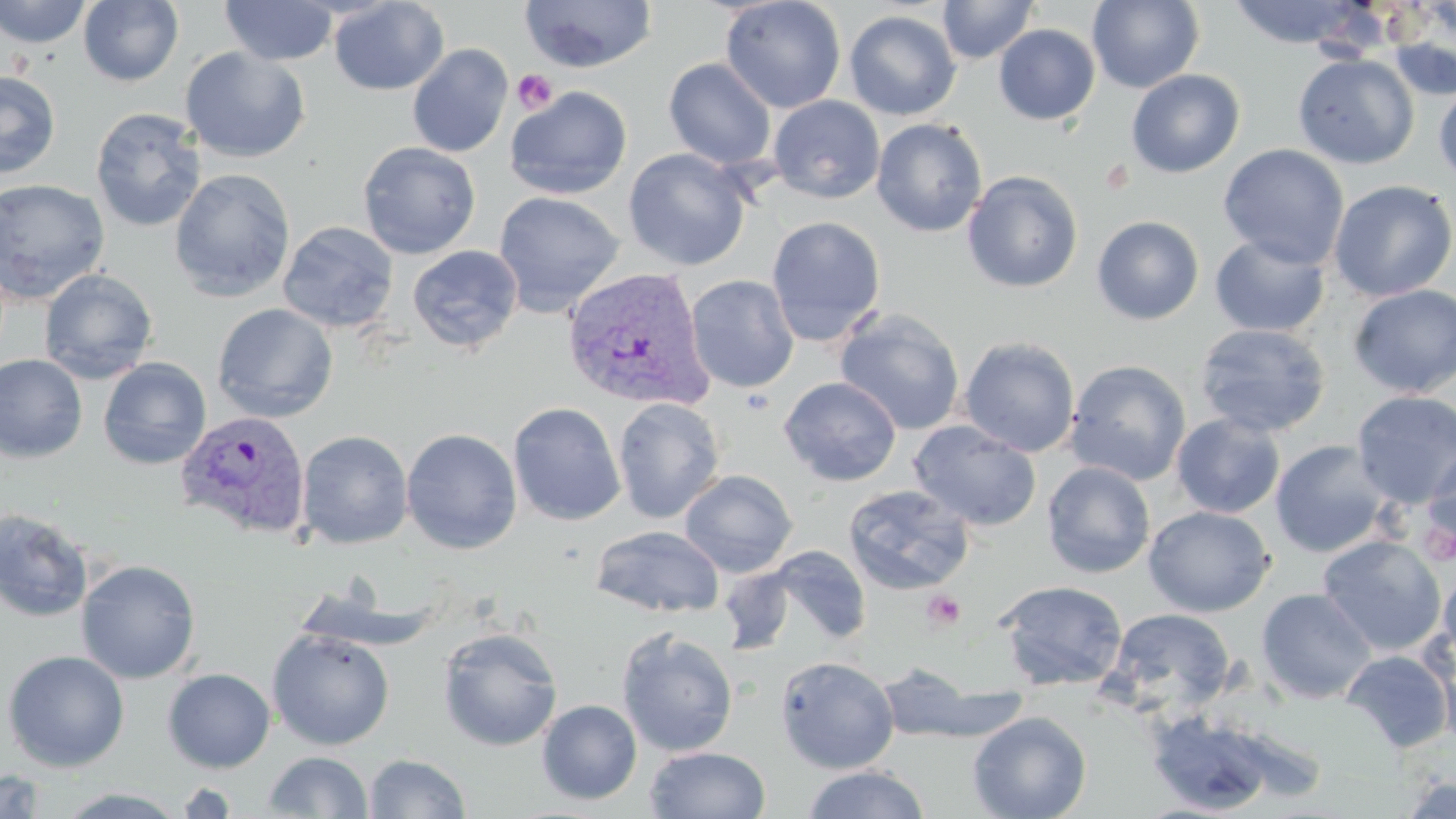
Approximate bounding boxes as (x1, y1, x2, y2) in pixels. Uninfected red blood cell locations: (0, 0, 93, 49), (77, 0, 183, 87), (328, 0, 449, 96), (519, 0, 657, 74), (720, 0, 846, 114), (937, 0, 1039, 65), (1087, 0, 1205, 94), (219, 1, 339, 66), (1228, 1, 1365, 48), (1385, 1, 1456, 100), (844, 9, 961, 120), (994, 24, 1100, 125), (407, 44, 513, 158), (180, 46, 311, 164), (1293, 53, 1419, 169), (663, 57, 777, 171), (1126, 69, 1245, 178), (1, 70, 60, 180), (1434, 83, 1456, 189), (505, 86, 632, 199), (768, 96, 884, 203), (90, 108, 207, 233), (871, 118, 988, 237), (357, 141, 482, 260), (1218, 144, 1350, 269), (622, 148, 752, 271), (169, 168, 295, 302), (961, 170, 1084, 293), (0, 179, 110, 304), (1328, 179, 1455, 302), (492, 190, 625, 317), (766, 216, 886, 346), (1092, 216, 1205, 325), (278, 221, 399, 333), (1092, 225, 1330, 328), (1209, 234, 1331, 337), (407, 245, 523, 354), (38, 269, 158, 384), (685, 275, 799, 393), (1348, 284, 1456, 398), (212, 303, 338, 423), (834, 308, 965, 435), (1194, 323, 1331, 437), (959, 336, 1081, 457), (0, 353, 88, 463), (98, 357, 212, 470), (1065, 359, 1191, 486), (779, 376, 902, 487), (1351, 390, 1456, 507), (612, 397, 725, 523), (508, 402, 626, 526), (1171, 413, 1285, 518), (909, 420, 1042, 531), (401, 428, 522, 555), (296, 430, 413, 550), (1269, 440, 1391, 558), (1422, 443, 1456, 553), (1041, 461, 1155, 578), (680, 469, 798, 577), (842, 484, 975, 596), (1144, 505, 1274, 617), (0, 508, 94, 623), (590, 525, 725, 618), (1316, 534, 1447, 656), (767, 546, 871, 647), (75, 559, 201, 684), (718, 565, 795, 655), (1438, 569, 1456, 671), (994, 580, 1129, 692), (1256, 588, 1377, 703), (1102, 607, 1236, 720), (266, 627, 395, 750), (438, 627, 563, 751), (616, 627, 739, 757), (1436, 639, 1456, 754), (1, 650, 130, 772), (1340, 650, 1454, 753), (775, 655, 899, 774), (871, 665, 1026, 744), (163, 669, 275, 773), (537, 699, 642, 805), (1143, 708, 1285, 815), (967, 711, 1092, 819), (645, 746, 771, 818), (263, 751, 373, 818), (364, 753, 471, 818), (801, 765, 931, 819), (0, 769, 50, 819), (1400, 777, 1455, 818), (175, 779, 241, 817), (50, 787, 192, 818). Plasmodium vivax-infected red blood cell locations: (562, 266, 715, 412), (174, 410, 313, 541). Platelet locations: (511, 69, 558, 113), (1417, 513, 1455, 567), (922, 589, 966, 632). Slide-level diagnosis: Plasmodium vivax. Single field of view. Image is 1456×819 pixels. Light microscopy. May-Grünwald-Giemsa stain. 1000x magnification. Thin blood film.